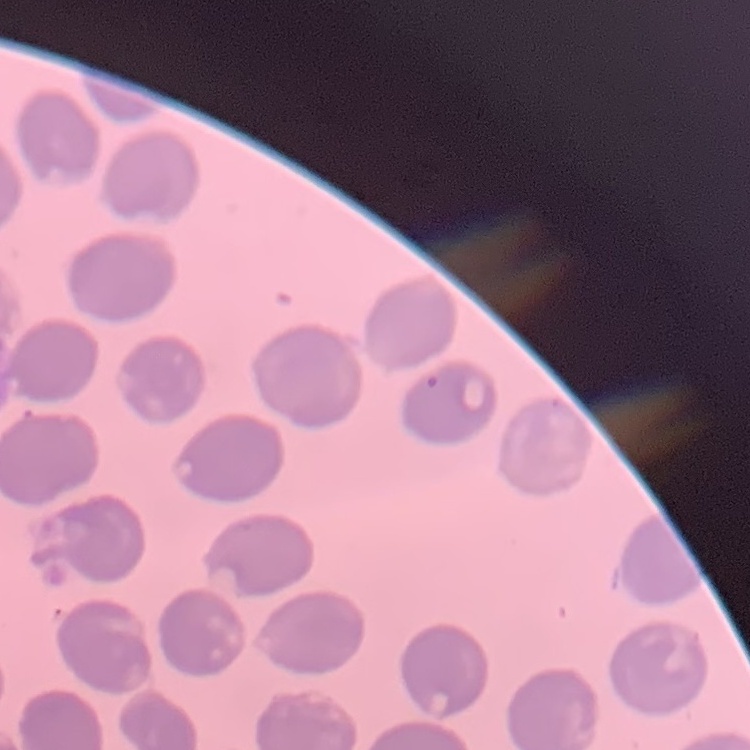
{
  "red_blood_cell_morphology": "no rouleaux formation",
  "stain": "Field's or Giemsa",
  "preparation": "thin blood film",
  "image_type": "one tile cut from a larger photomicrograph"
}